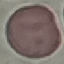
result = no malaria parasites detected
image type = automatically extracted cell patch, resized to 64 × 64 pixels
preparation = thin blood film
capture = smartphone camera at the microscope eyepiece
stain = Giemsa